Report the malaria status of this cell.
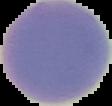
It is uninfected.

image type = segmented cell region with the area outside set to black
image size = 112×106 pixels
preparation = thin blood film